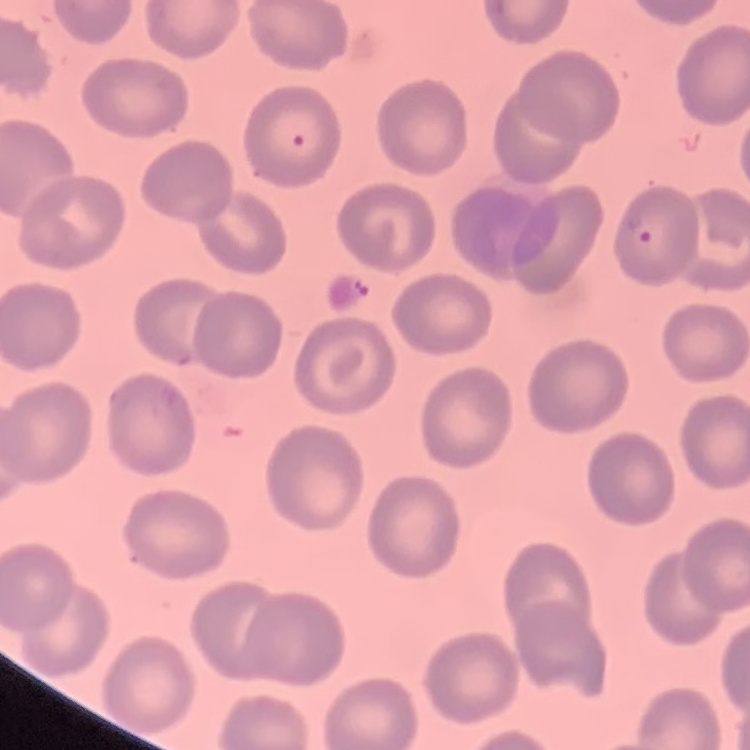

erythrocyte_morphology: no rouleaux formation
image_type: square crop of a larger photomicrograph
preparation: thin peripheral smear
stain: Field's or Giemsa